Locate every blood parasite and identify its species.
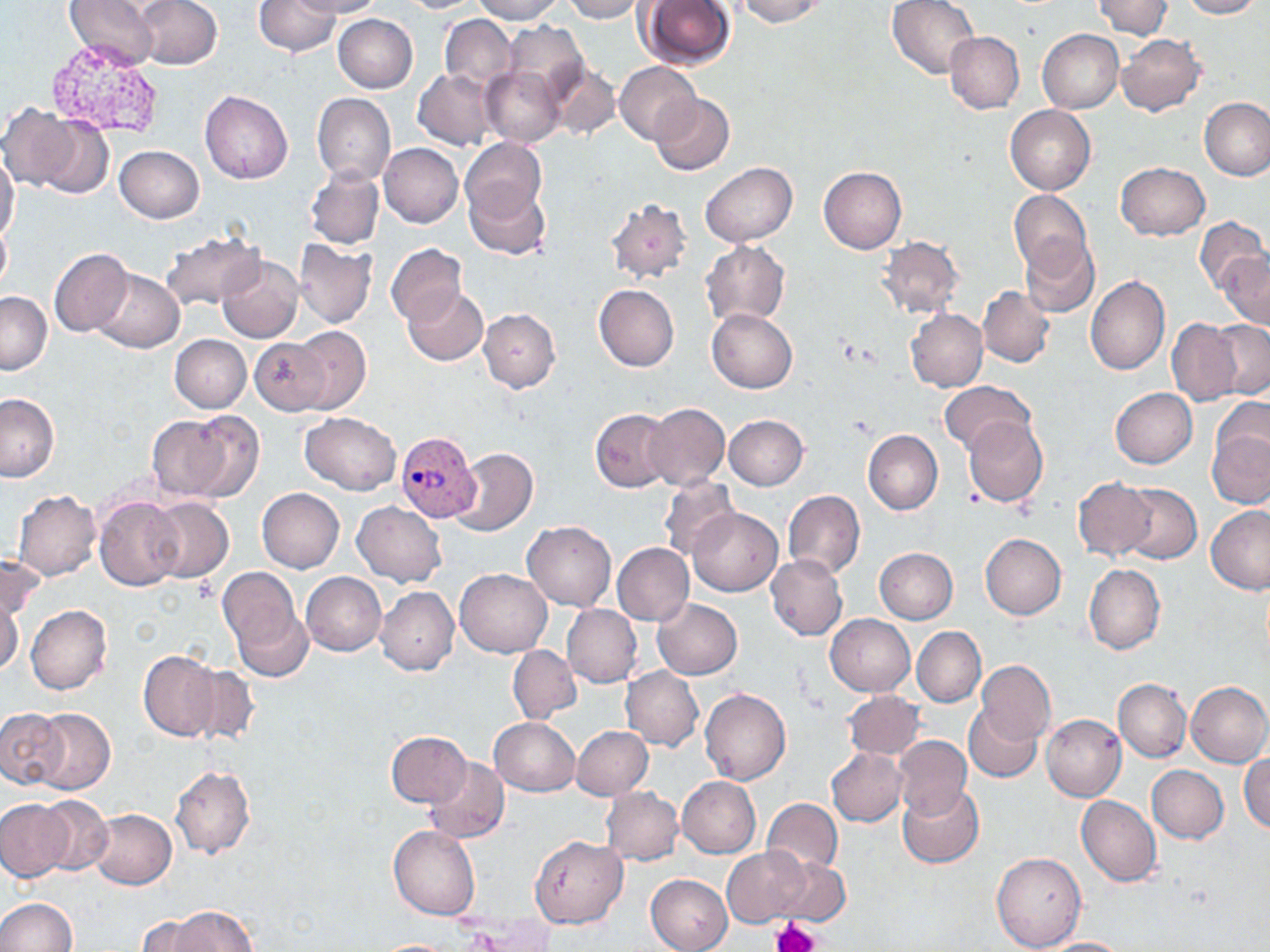
Approximate bounding boxes as (x1, y1, x2, y2) in pixels.
Plasmodium vivax-infected red blood cells: (395, 431, 480, 522).
No Plasmodium falciparum, Plasmodium ovale, Plasmodium malariae, Babesia divergens, or Trypanosoma brucei observed.

Summary:
  - Platelet locations: (771, 918, 817, 952)
  - Uninfected red blood cell locations: (65, 0, 164, 69), (134, 0, 221, 69), (296, 0, 384, 17), (398, 0, 485, 13), (469, 0, 564, 23), (561, 0, 648, 23), (737, 0, 825, 28), (886, 0, 979, 80), (1092, 0, 1172, 38), (1179, 0, 1262, 19), (253, 1, 339, 56), (639, 1, 736, 70), (333, 14, 418, 93), (439, 14, 516, 93), (499, 22, 590, 104), (1036, 29, 1123, 114), (945, 31, 1025, 114), (1117, 34, 1207, 117), (613, 61, 700, 143), (546, 64, 621, 141), (481, 66, 564, 147), (413, 69, 498, 151), (200, 90, 294, 184), (650, 92, 735, 176), (312, 93, 395, 184), (1201, 98, 1270, 181), (0, 103, 83, 191), (1005, 106, 1096, 194), (34, 114, 113, 198), (460, 137, 548, 219), (378, 143, 463, 228), (115, 146, 204, 223), (0, 151, 20, 246), (1115, 162, 1210, 241), (701, 163, 796, 247), (818, 166, 906, 254), (305, 167, 384, 249), (466, 180, 551, 259), (1009, 190, 1093, 276), (606, 197, 694, 285), (1194, 216, 1268, 295), (0, 221, 11, 294), (158, 229, 265, 311), (877, 235, 964, 319), (1020, 237, 1100, 318), (294, 240, 377, 328), (701, 240, 790, 326), (386, 243, 466, 326), (49, 247, 133, 337), (1220, 252, 1270, 330), (216, 254, 303, 343), (90, 269, 184, 353), (1086, 275, 1170, 375), (594, 284, 679, 372), (402, 286, 488, 366), (978, 286, 1055, 367), (0, 291, 52, 374), (479, 308, 560, 392), (906, 308, 988, 392), (707, 309, 798, 393), (1167, 318, 1243, 406), (1208, 321, 1269, 400), (288, 325, 371, 415), (171, 334, 251, 413), (248, 337, 330, 416), (939, 380, 1035, 454), (1110, 387, 1197, 469), (0, 393, 60, 481), (642, 402, 730, 489), (591, 409, 673, 492), (1207, 409, 1270, 509), (183, 410, 266, 503), (299, 412, 402, 494), (724, 415, 808, 489), (962, 415, 1047, 508), (146, 416, 238, 501), (862, 430, 942, 515), (451, 448, 538, 536), (657, 474, 740, 563), (1073, 476, 1155, 560), (256, 488, 345, 573), (782, 490, 864, 579), (12, 491, 102, 580), (95, 495, 184, 591), (147, 497, 232, 580), (352, 500, 446, 586), (1206, 505, 1270, 594), (688, 507, 782, 596), (521, 521, 616, 611), (979, 532, 1066, 620), (612, 543, 694, 625), (874, 547, 958, 623), (1, 554, 43, 626), (765, 554, 846, 641), (1084, 563, 1165, 654), (218, 567, 303, 653), (455, 568, 552, 658), (301, 572, 386, 656), (375, 587, 459, 675), (0, 589, 24, 678), (652, 599, 742, 679), (232, 603, 312, 683), (25, 604, 112, 693), (562, 605, 643, 687), (825, 614, 915, 696), (508, 624, 635, 714), (912, 626, 986, 706), (508, 646, 580, 722), (138, 652, 222, 741), (975, 659, 1055, 745), (184, 664, 261, 745), (621, 667, 703, 752), (1113, 678, 1191, 762), (1185, 681, 1270, 767), (700, 688, 792, 784), (842, 691, 925, 759), (964, 703, 1044, 782), (0, 705, 68, 790), (31, 707, 115, 795), (1040, 714, 1127, 801), (489, 717, 580, 796), (571, 726, 653, 799), (385, 731, 472, 808), (893, 735, 972, 817), (827, 749, 908, 826), (1240, 754, 1270, 833), (424, 756, 509, 843), (169, 765, 255, 860), (1146, 766, 1228, 844), (678, 777, 760, 857), (898, 783, 984, 868), (600, 787, 684, 865), (36, 795, 114, 876), (1076, 795, 1160, 886), (0, 798, 73, 880), (761, 798, 843, 876), (87, 809, 177, 889), (388, 825, 480, 921), (529, 835, 628, 928), (721, 846, 815, 928), (992, 850, 1087, 951), (771, 857, 850, 928), (645, 874, 733, 952), (0, 897, 75, 951), (169, 906, 259, 951), (136, 914, 218, 952), (1035, 937, 1134, 951), (369, 939, 467, 951)
  - Slide-level diagnosis: Plasmodium vivax
  - Magnification: 1000x
  - Stain: May-Grünwald-Giemsa
  - Field of view: single
  - Preparation: thin blood smear
  - Modality: optical microscopy
  - Image size: 1270×952 pixels